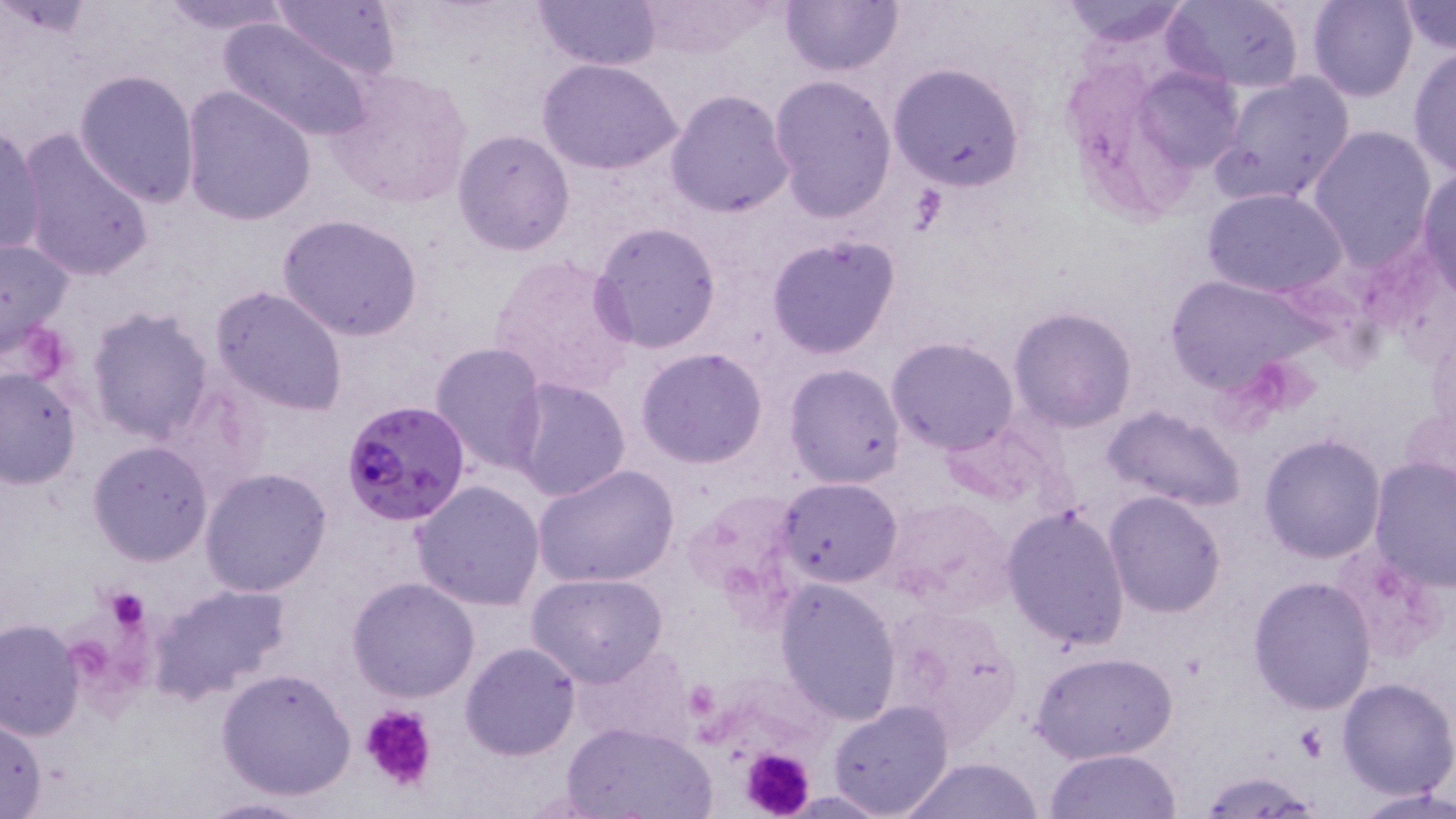

Summary:
  - Coordinate format: approximate bounding boxes as named x1/y1/x2/y2 corners in pixels
  - Platelet locations: (x1=100, y1=584, x2=153, y2=629), (x1=360, y1=704, x2=440, y2=794), (x1=1296, y1=724, x2=1331, y2=761), (x1=739, y1=746, x2=816, y2=819)
  - Plasmodium falciparum-infected red blood cell locations: (x1=341, y1=397, x2=472, y2=528)
  - Uninfected red blood cell locations: (x1=151, y1=0, x2=297, y2=35), (x1=271, y1=0, x2=404, y2=82), (x1=533, y1=0, x2=660, y2=69), (x1=637, y1=0, x2=779, y2=56), (x1=779, y1=0, x2=906, y2=77), (x1=1054, y1=0, x2=1197, y2=47), (x1=1163, y1=0, x2=1306, y2=91), (x1=1307, y1=0, x2=1418, y2=101), (x1=1396, y1=1, x2=1456, y2=54), (x1=217, y1=14, x2=374, y2=145), (x1=1407, y1=45, x2=1456, y2=180), (x1=1142, y1=50, x2=1245, y2=173), (x1=536, y1=57, x2=684, y2=175), (x1=887, y1=62, x2=1026, y2=191), (x1=324, y1=67, x2=474, y2=210), (x1=74, y1=68, x2=201, y2=206), (x1=1213, y1=71, x2=1356, y2=207), (x1=767, y1=75, x2=897, y2=223), (x1=181, y1=85, x2=316, y2=227), (x1=664, y1=89, x2=795, y2=219), (x1=0, y1=124, x2=45, y2=259), (x1=1307, y1=125, x2=1438, y2=267), (x1=15, y1=128, x2=156, y2=283), (x1=452, y1=129, x2=576, y2=256), (x1=1417, y1=169, x2=1456, y2=296), (x1=1200, y1=186, x2=1348, y2=298), (x1=278, y1=213, x2=422, y2=340), (x1=590, y1=220, x2=724, y2=356), (x1=765, y1=234, x2=903, y2=359), (x1=0, y1=235, x2=77, y2=360), (x1=487, y1=252, x2=639, y2=400), (x1=1163, y1=272, x2=1326, y2=398), (x1=212, y1=285, x2=348, y2=416), (x1=1008, y1=305, x2=1138, y2=432), (x1=84, y1=306, x2=216, y2=446), (x1=885, y1=337, x2=1019, y2=456), (x1=429, y1=343, x2=550, y2=474), (x1=635, y1=347, x2=769, y2=468), (x1=784, y1=363, x2=907, y2=487), (x1=0, y1=364, x2=81, y2=488), (x1=507, y1=377, x2=631, y2=502), (x1=1103, y1=406, x2=1246, y2=514), (x1=938, y1=417, x2=1062, y2=510), (x1=1258, y1=433, x2=1386, y2=562), (x1=86, y1=440, x2=213, y2=567), (x1=1369, y1=459, x2=1455, y2=592), (x1=532, y1=462, x2=679, y2=590), (x1=200, y1=467, x2=332, y2=596), (x1=776, y1=477, x2=903, y2=589), (x1=410, y1=479, x2=548, y2=612), (x1=1102, y1=489, x2=1228, y2=619), (x1=1001, y1=505, x2=1132, y2=652), (x1=1331, y1=544, x2=1449, y2=665), (x1=525, y1=572, x2=669, y2=686), (x1=1248, y1=576, x2=1379, y2=714), (x1=347, y1=577, x2=480, y2=702), (x1=773, y1=577, x2=903, y2=724), (x1=148, y1=581, x2=293, y2=704), (x1=0, y1=617, x2=84, y2=741), (x1=459, y1=641, x2=581, y2=761), (x1=569, y1=642, x2=695, y2=748), (x1=1032, y1=650, x2=1178, y2=765), (x1=216, y1=667, x2=357, y2=801), (x1=1337, y1=676, x2=1456, y2=799), (x1=827, y1=700, x2=954, y2=818), (x1=0, y1=712, x2=48, y2=819), (x1=560, y1=720, x2=719, y2=819), (x1=1045, y1=748, x2=1184, y2=819), (x1=897, y1=758, x2=1050, y2=818), (x1=1196, y1=773, x2=1323, y2=815), (x1=1354, y1=786, x2=1456, y2=819), (x1=194, y1=796, x2=317, y2=818)
  - Slide-level diagnosis: Plasmodium falciparum
  - Preparation: thin blood smear
  - Image size: 1456×819 pixels
  - Modality: light microscopy
  - Stain: May-Grünwald-Giemsa
  - Field of view: one of a larger specimen
  - Magnification: 1000x